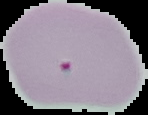
image size = 148×115 pixels
image type = segmented cell region on a black background
malaria status = uninfected
preparation = thin blood film